Identify the blood parasite species.
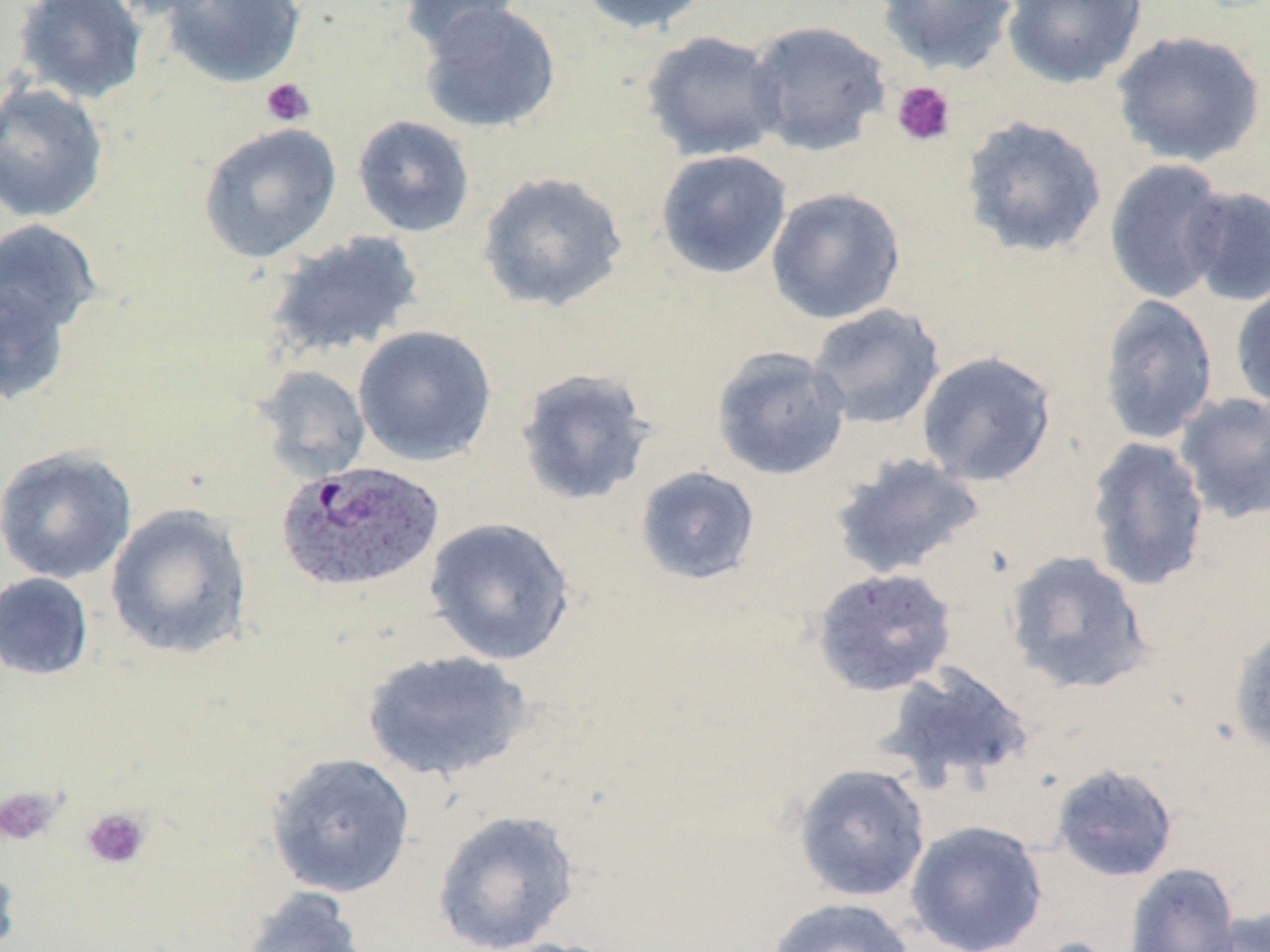

Plasmodium ovale.

Summary:
  - Coordinate format: approximate bounding boxes as (x1,y1)-(x2,y2) corner pairs in pixels
  - Plasmodium ovale-infected red blood cell locations: (275,460)-(444,594)
  - Uninfected red blood cell locations: (12,0)-(149,104), (104,0)-(229,20), (160,0)-(307,88), (400,0)-(530,54), (575,0)-(714,35), (876,0)-(1019,75), (1001,0)-(1146,89), (417,1)-(561,135), (745,20)-(892,156), (640,30)-(786,161), (1110,30)-(1266,167), (0,82)-(110,224), (959,114)-(1108,259), (352,115)-(475,238), (198,123)-(342,264), (655,149)-(793,279), (1104,158)-(1231,304), (477,170)-(629,313), (1181,185)-(1270,306), (766,186)-(906,325), (0,219)-(102,338), (265,230)-(426,360), (0,276)-(73,407), (1230,280)-(1270,412), (1098,294)-(1218,446), (806,303)-(946,431), (352,325)-(498,467), (711,346)-(851,481), (917,351)-(1058,488), (252,364)-(372,482), (515,367)-(655,506), (1173,391)-(1270,524), (1084,435)-(1211,592), (0,445)-(137,584), (828,452)-(987,581), (635,465)-(761,586), (106,504)-(253,659), (424,517)-(576,665), (1003,549)-(1153,696), (811,567)-(958,697), (0,572)-(94,681), (1228,620)-(1270,756), (361,649)-(534,783), (877,661)-(1035,792), (266,751)-(416,898), (793,762)-(931,902), (1050,763)-(1179,882), (432,809)-(579,952), (905,819)-(1048,952), (0,852)-(21,952), (1123,862)-(1242,952), (241,887)-(372,952), (766,896)-(917,952), (1200,907)-(1270,952)
  - Platelet locations: (261,78)-(315,127), (891,80)-(956,147), (0,787)-(60,846), (81,807)-(151,870)
  - Image size: 1270×952 pixels
  - Preparation: thin blood film
  - Stain: May-Grünwald-Giemsa
  - Magnification: 1000x
  - Modality: light microscopy
  - Field of view: one of a larger specimen